Classify this cell by malaria status.
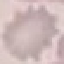

Uninfected.

Summary:
  - Preparation: thin blood film
  - Capture: smartphone camera at the microscope eyepiece
  - Stain: Giemsa
  - Image type: cell patch, automatically extracted from a larger field of view and resized to 64 × 64 pixels